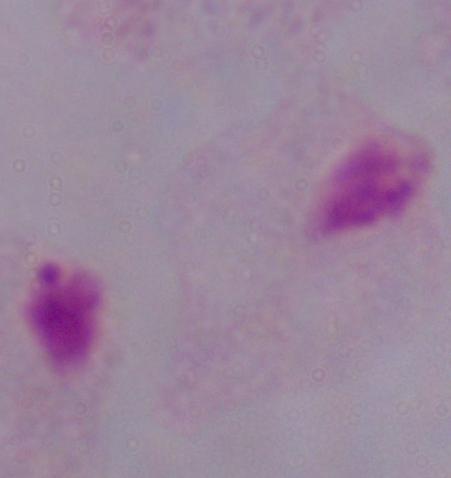 Micrograph. A trichomonad is seen. Captured at 1000x magnification.